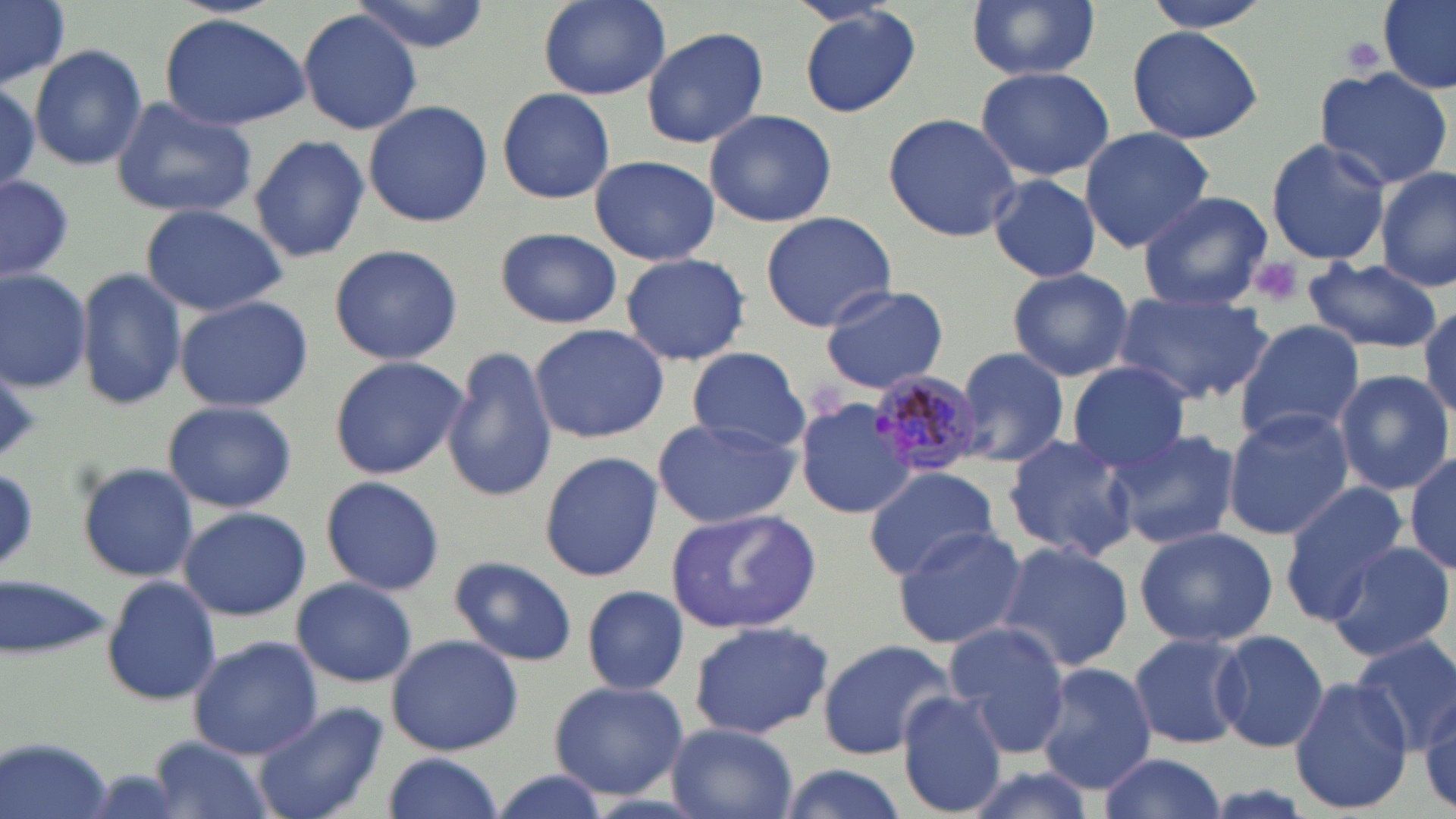
slide-level diagnosis = Plasmodium malariae
platelet locations = approximate bounding boxes as (x1,y1)-(x2,y2) corner pairs in pixels: (1339,36)-(1389,75), (1249,255)-(1304,305), (0,369)-(43,460)
image size = 1456×819 pixels
stain = May-Grünwald-Giemsa
field of view = single
uninfected red blood cell locations = approximate bounding boxes as (x1,y1)-(x2,y2) corner pairs in pixels: (0,0)-(72,87), (349,0)-(490,53), (538,0)-(670,100), (965,0)-(1101,81), (1141,0)-(1276,32), (1379,0)-(1456,95), (796,5)-(923,118), (296,9)-(422,136), (158,12)-(310,131), (1126,24)-(1262,145), (640,25)-(769,150), (28,43)-(147,171), (1104,43)-(1247,222), (1314,65)-(1455,191), (975,66)-(1114,181), (0,78)-(47,196), (496,87)-(615,204), (107,96)-(260,218), (363,99)-(492,230), (703,108)-(838,228), (884,113)-(1024,242), (1079,127)-(1214,250), (249,133)-(370,265), (1263,137)-(1391,265), (590,154)-(719,266), (1375,166)-(1456,292), (987,173)-(1102,283), (0,177)-(75,283), (1137,192)-(1273,311), (137,202)-(291,316), (760,211)-(897,333), (493,227)-(622,329), (327,244)-(465,366), (620,251)-(752,367), (1304,259)-(1443,352), (0,266)-(92,391), (77,267)-(186,411), (1007,267)-(1134,382), (818,284)-(950,394), (1115,290)-(1272,408), (173,294)-(313,413), (1417,301)-(1455,422), (1234,320)-(1364,442), (528,323)-(669,443), (535,337)-(669,557), (442,346)-(556,502), (687,346)-(809,452), (952,347)-(1068,468), (328,355)-(466,481), (1064,364)-(1191,475), (1334,369)-(1456,496), (867,370)-(986,476), (794,394)-(918,522), (161,399)-(299,514), (1222,409)-(1354,539), (651,414)-(802,529), (1107,428)-(1241,551), (1004,434)-(1140,564), (1406,449)-(1456,574), (538,451)-(663,581), (75,462)-(201,582), (0,466)-(41,573), (863,466)-(1002,575), (321,476)-(444,595), (1281,482)-(1409,624), (178,505)-(311,622), (665,507)-(821,634), (891,525)-(1028,649), (1133,525)-(1280,647), (990,541)-(1135,675), (1326,541)-(1455,665), (449,556)-(578,667), (102,575)-(221,706), (1,576)-(114,661), (291,577)-(418,688), (582,585)-(690,694), (686,619)-(835,741), (943,622)-(1072,757), (1212,629)-(1328,753), (1128,631)-(1248,750), (386,633)-(523,755), (186,636)-(323,760), (1350,638)-(1456,755), (816,640)-(956,759), (1035,662)-(1157,794), (1289,675)-(1414,814), (546,680)-(690,799), (1409,687)-(1456,807), (896,690)-(1009,817), (253,699)-(390,819), (665,722)-(800,819), (146,734)-(276,819), (2,737)-(116,819), (1095,751)-(1228,819), (380,753)-(503,819), (773,763)-(912,819), (957,764)-(1102,819), (484,768)-(618,819)
modality = light microscopy
magnification = 1000x
preparation = thin blood film